Assess the morphology of the red blood cells.
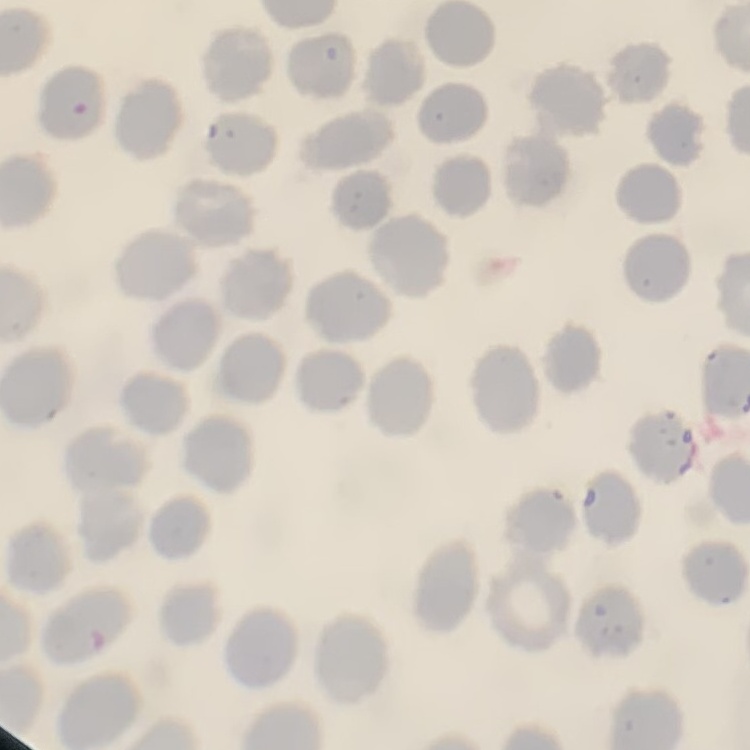
No rouleaux formation.

Summary:
  - Image type: one tile cut from a larger photomicrograph
  - Preparation: thin blood smear
  - Stain: Field's or Giemsa